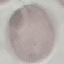
Summary:
  - Result: no malaria parasites seen
  - Image type: cell patch, automatically extracted from a larger field of view and resized to 64 × 64 pixels
  - Stain: Giemsa
  - Preparation: thin smear
  - Capture: smartphone camera at the microscope eyepiece